Outline each blood parasite and name the species.
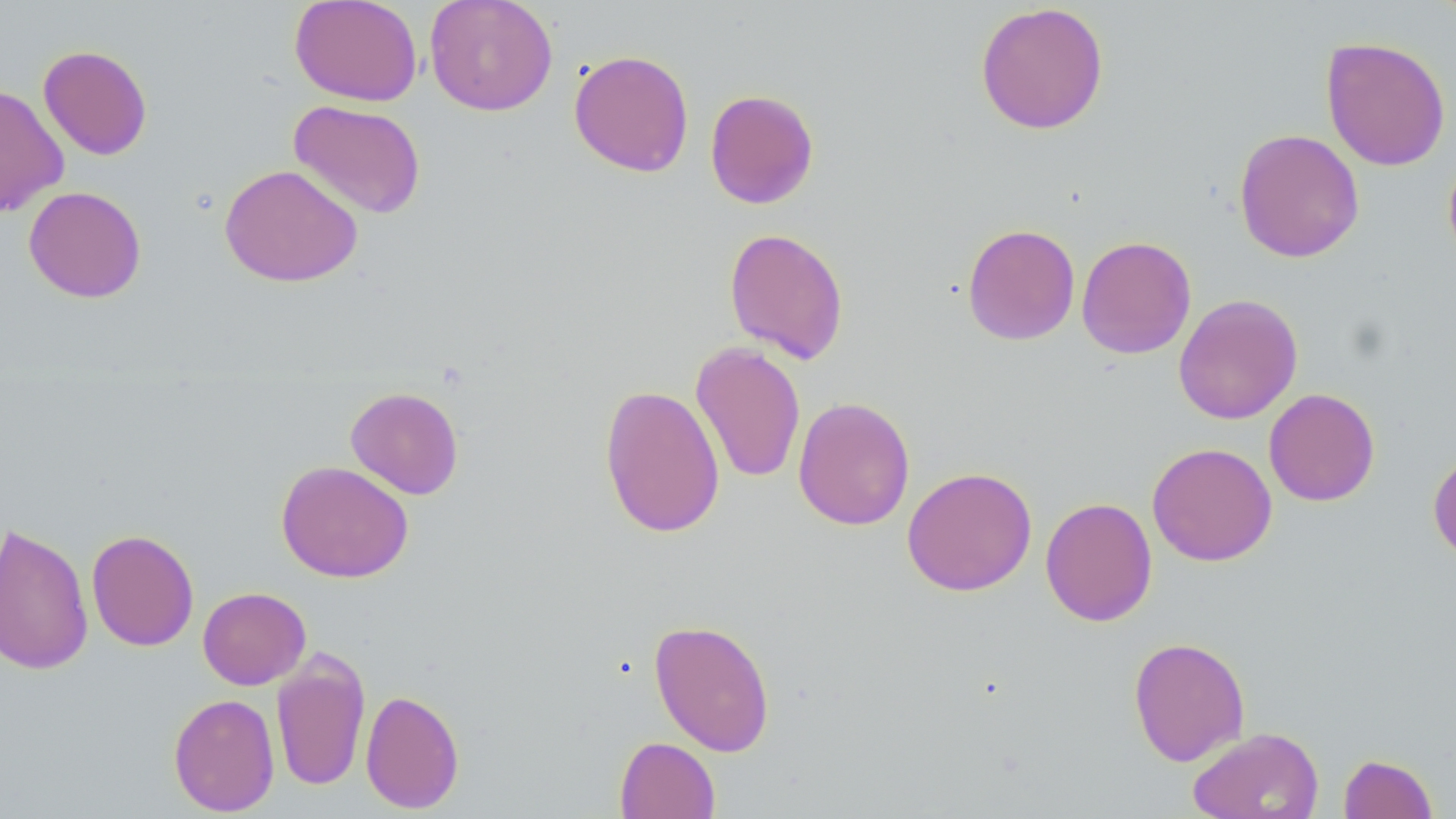

No blood parasites observed.

{
  "slide_level_diagnosis": "no evidence of blood parasites",
  "field_of_view": "one of a larger specimen",
  "uninfected_red_blood_cell_locations": "approximate bounding boxes as (x1,y1)-(x2,y2) corner pairs in pixels: (289,0)-(423,106), (424,0)-(558,116), (974,2)-(1110,135), (1320,36)-(1451,172), (38,45)-(153,160), (569,49)-(694,177), (0,83)-(69,217), (705,89)-(819,209), (287,99)-(427,220), (1233,128)-(1364,263), (1442,152)-(1456,269), (219,163)-(363,288), (23,186)-(147,303), (962,223)-(1080,346), (723,227)-(849,364), (1076,236)-(1197,359), (1173,294)-(1303,424), (690,341)-(806,484), (599,383)-(725,539), (345,386)-(464,499), (1263,388)-(1380,506), (793,396)-(915,531), (1147,442)-(1277,566), (1428,446)-(1456,566), (276,460)-(414,583), (901,466)-(1037,597), (1040,496)-(1158,627), (0,522)-(94,676), (86,529)-(199,652), (197,587)-(311,690), (649,619)-(776,756), (1128,636)-(1251,767), (271,649)-(371,792), (360,689)-(465,814), (168,693)-(280,816), (1187,727)-(1324,819), (614,736)-(720,819), (1338,753)-(1438,818)",
  "image_size": "1456×819 pixels",
  "modality": "optical microscopy",
  "magnification": "1000x",
  "preparation": "thin blood smear",
  "stain": "May-Grünwald-Giemsa"
}